Identify the parasite.
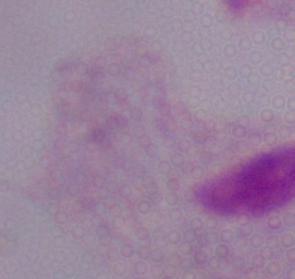
A trichomonad.

modality = photomicrograph
magnification = 1000x